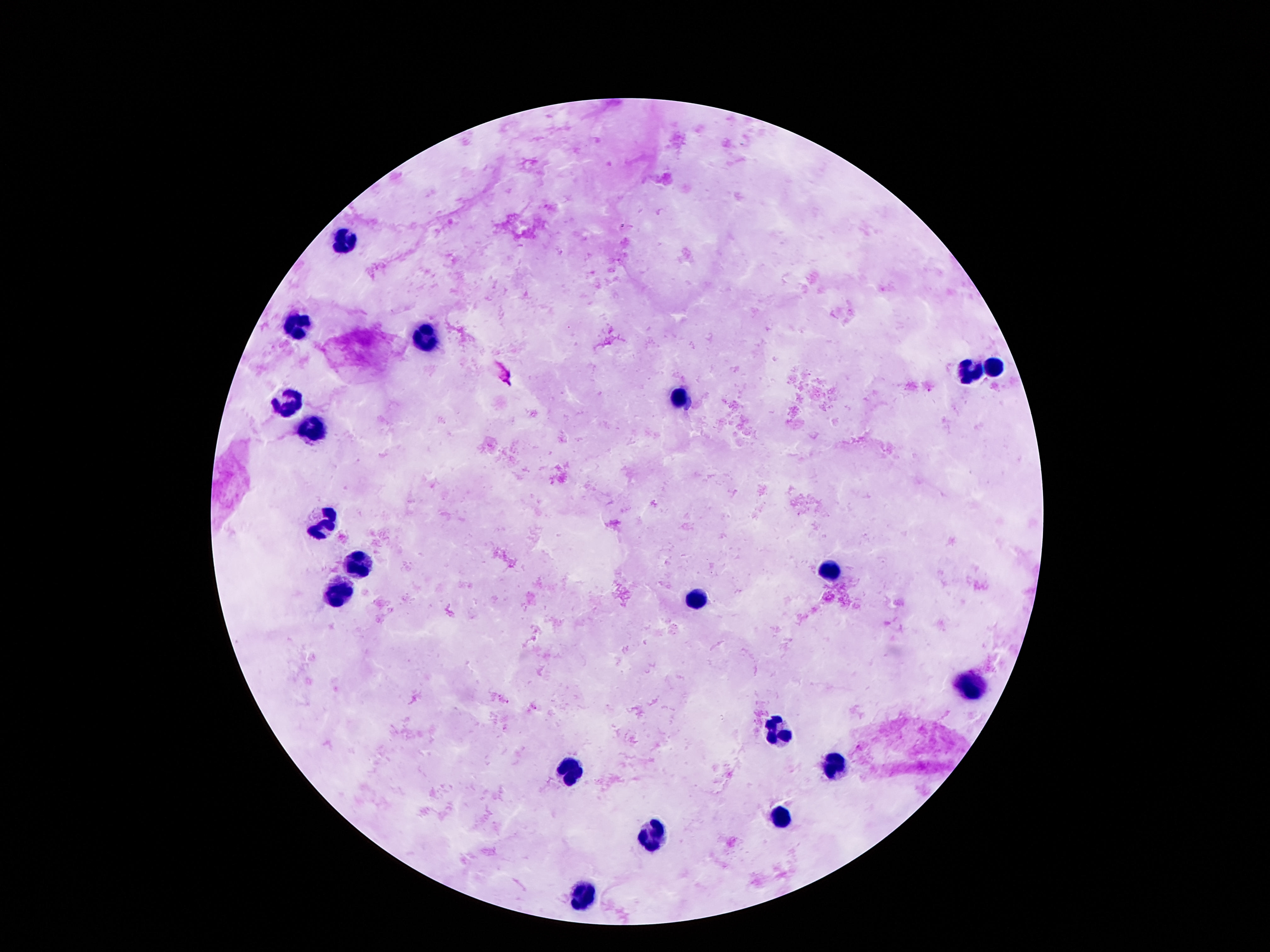
Approximate centers as {x, y} in pixels.
Summary:
  - Leukocyte locations: {345, 245}, {296, 326}, {425, 337}, {994, 366}, {970, 372}, {679, 400}, {284, 404}, {308, 429}, {324, 524}, {354, 564}, {826, 567}, {340, 594}, {700, 599}, {970, 684}, {777, 730}, {835, 767}, {569, 770}, {781, 819}, {651, 835}, {581, 898}
  - Magnification: 100x
  - Capture: smartphone camera through the microscope eyepiece
  - Preparation: thick blood smear
  - Patient malaria status: uninfected
  - Stain: Giemsa
  - Field of view: one from this slide
  - Image size: 1270×952 pixels